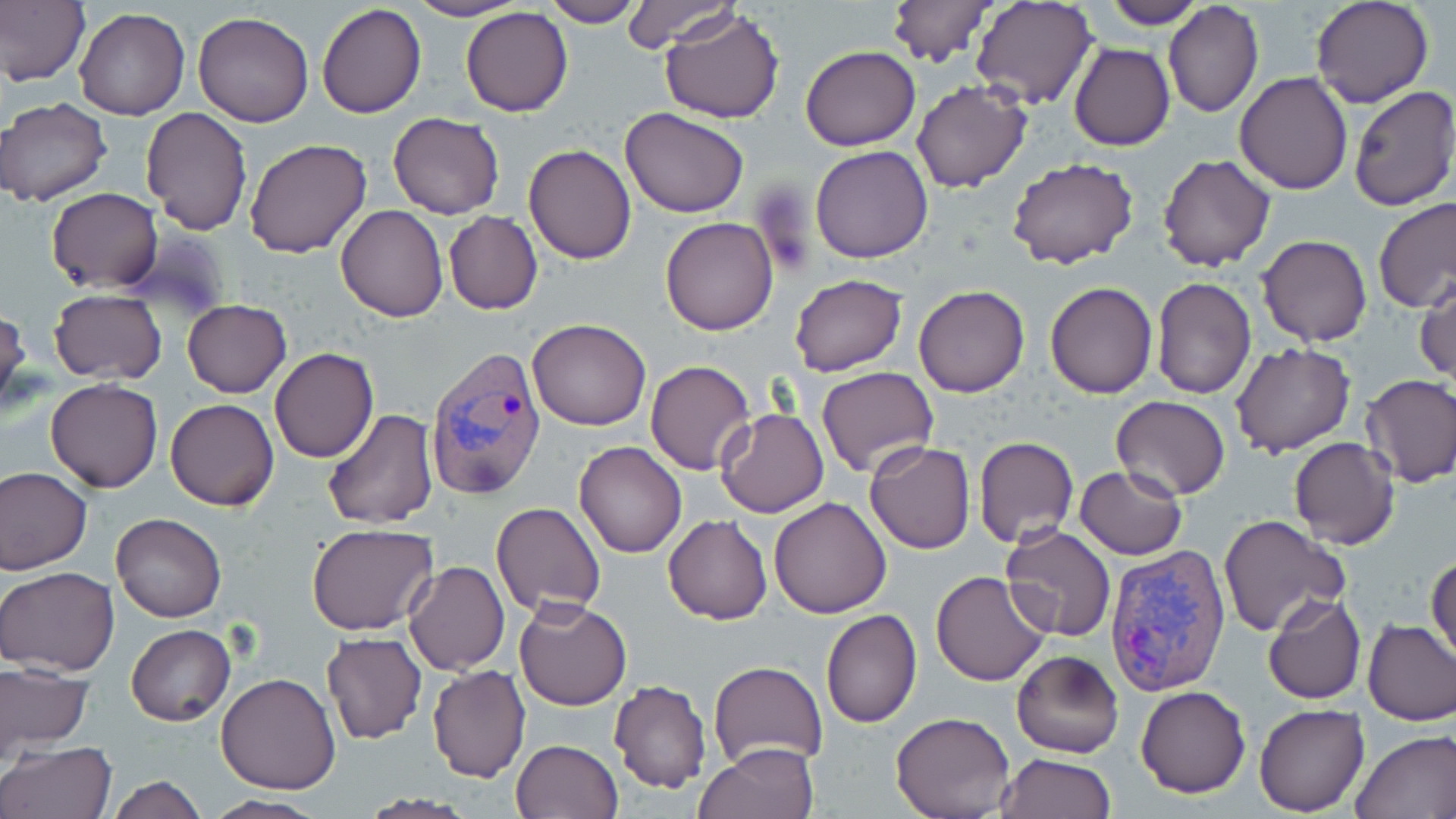

Approximate bounding boxes as named x1/y1/x2/y2 corners in pixels. Uninfected red blood cell locations: (x1=0, y1=0, x2=90, y2=89), (x1=406, y1=0, x2=528, y2=22), (x1=539, y1=0, x2=642, y2=26), (x1=621, y1=0, x2=737, y2=53), (x1=885, y1=0, x2=994, y2=67), (x1=1100, y1=0, x2=1205, y2=27), (x1=1309, y1=0, x2=1435, y2=108), (x1=971, y1=2, x2=1096, y2=110), (x1=316, y1=3, x2=426, y2=118), (x1=1163, y1=3, x2=1263, y2=118), (x1=74, y1=7, x2=189, y2=120), (x1=460, y1=7, x2=572, y2=116), (x1=659, y1=8, x2=784, y2=124), (x1=193, y1=10, x2=315, y2=127), (x1=1069, y1=43, x2=1176, y2=151), (x1=800, y1=45, x2=919, y2=150), (x1=1234, y1=70, x2=1353, y2=195), (x1=911, y1=80, x2=1033, y2=193), (x1=1347, y1=86, x2=1456, y2=212), (x1=2, y1=98, x2=113, y2=207), (x1=620, y1=106, x2=750, y2=218), (x1=138, y1=107, x2=252, y2=234), (x1=388, y1=111, x2=505, y2=220), (x1=244, y1=137, x2=373, y2=259), (x1=523, y1=144, x2=636, y2=263), (x1=809, y1=146, x2=933, y2=263), (x1=1156, y1=154, x2=1276, y2=273), (x1=1008, y1=158, x2=1138, y2=271), (x1=46, y1=187, x2=163, y2=293), (x1=1372, y1=197, x2=1456, y2=312), (x1=335, y1=204, x2=449, y2=322), (x1=444, y1=212, x2=543, y2=314), (x1=660, y1=217, x2=780, y2=336), (x1=1258, y1=234, x2=1373, y2=348), (x1=1416, y1=273, x2=1456, y2=385), (x1=790, y1=275, x2=907, y2=376), (x1=1151, y1=277, x2=1257, y2=398), (x1=1045, y1=283, x2=1158, y2=399), (x1=914, y1=285, x2=1029, y2=398), (x1=48, y1=288, x2=167, y2=384), (x1=182, y1=299, x2=292, y2=398), (x1=0, y1=307, x2=30, y2=419), (x1=527, y1=319, x2=652, y2=432), (x1=1230, y1=342, x2=1356, y2=459), (x1=270, y1=347, x2=378, y2=463), (x1=646, y1=360, x2=755, y2=474), (x1=816, y1=366, x2=939, y2=478), (x1=1360, y1=373, x2=1456, y2=488), (x1=45, y1=378, x2=163, y2=493), (x1=1111, y1=394, x2=1231, y2=500), (x1=166, y1=398, x2=279, y2=511), (x1=715, y1=407, x2=830, y2=518), (x1=321, y1=408, x2=438, y2=530), (x1=974, y1=436, x2=1078, y2=549), (x1=1289, y1=438, x2=1399, y2=549), (x1=865, y1=440, x2=975, y2=553), (x1=574, y1=441, x2=686, y2=558), (x1=1076, y1=466, x2=1186, y2=561), (x1=0, y1=467, x2=91, y2=575), (x1=769, y1=497, x2=892, y2=619), (x1=492, y1=502, x2=607, y2=618), (x1=111, y1=512, x2=227, y2=623), (x1=662, y1=515, x2=773, y2=625), (x1=1221, y1=516, x2=1347, y2=639), (x1=1000, y1=523, x2=1117, y2=642), (x1=307, y1=524, x2=439, y2=635), (x1=1427, y1=550, x2=1455, y2=664), (x1=404, y1=560, x2=511, y2=676), (x1=1, y1=566, x2=120, y2=677), (x1=930, y1=570, x2=1050, y2=685), (x1=1262, y1=593, x2=1366, y2=704), (x1=514, y1=598, x2=632, y2=710), (x1=821, y1=608, x2=923, y2=727), (x1=1362, y1=618, x2=1456, y2=725), (x1=126, y1=624, x2=234, y2=726), (x1=321, y1=633, x2=427, y2=743), (x1=1010, y1=648, x2=1126, y2=759), (x1=709, y1=660, x2=828, y2=771), (x1=0, y1=663, x2=92, y2=759), (x1=427, y1=666, x2=530, y2=782), (x1=216, y1=673, x2=341, y2=793), (x1=609, y1=680, x2=712, y2=794), (x1=1137, y1=685, x2=1251, y2=798), (x1=1254, y1=703, x2=1369, y2=816), (x1=891, y1=710, x2=1016, y2=818), (x1=1350, y1=729, x2=1456, y2=818), (x1=511, y1=738, x2=622, y2=819), (x1=1, y1=741, x2=117, y2=819), (x1=697, y1=742, x2=821, y2=819), (x1=996, y1=753, x2=1116, y2=818), (x1=107, y1=775, x2=208, y2=818), (x1=200, y1=794, x2=326, y2=818), (x1=358, y1=794, x2=477, y2=817). Plasmodium vivax-infected red blood cell locations: (x1=424, y1=347, x2=548, y2=498), (x1=1103, y1=545, x2=1230, y2=695). Slide-level diagnosis: Plasmodium vivax. Thin blood smear. Single field of view. Image is 1456×819 pixels. May-Grünwald-Giemsa-stained preparation. Light microscopy. Captured at 1000x magnification.